Report the malaria status of this cell.
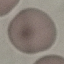

Uninfected.

Thin smear of blood. Acquired by smartphone through the microscope eyepiece. Automatically extracted cell patch, resized to 64 × 64 pixels. Giemsa-stained preparation.